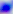

Toxoplasma gondii is shown. Photomicrograph. 400x magnification.